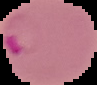

image type = cell region segmented out of the field of view; surrounding area masked to black
preparation = thin blood smear
malaria status = parasitized
image size = 97×85 pixels